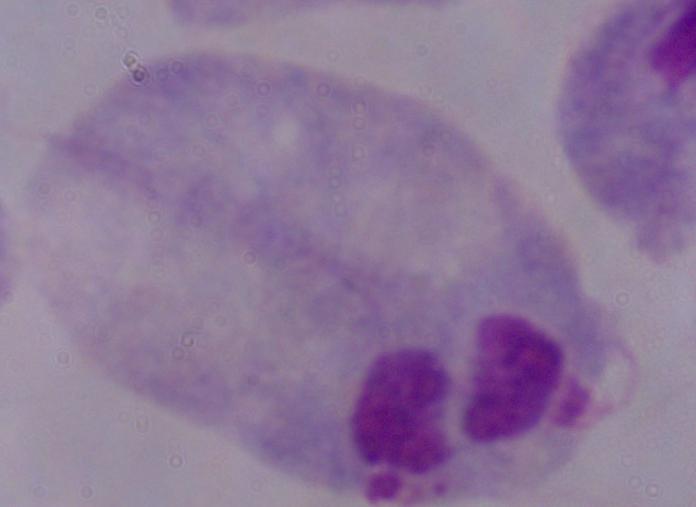
{
  "identification": "trichomonad",
  "magnification": "1000x",
  "modality": "micrograph"
}